Classify this cell by malaria status.
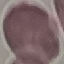
Uninfected.

image type = automatically extracted cell patch, resized to 64 × 64 pixels
capture = smartphone camera at the microscope eyepiece
stain = Giemsa
preparation = thin blood smear